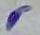
magnification = 1000x
modality = micrograph
identification = Toxoplasma gondii